State which parasite is depicted.
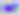
Toxoplasma gondii.

Micrograph. Captured at 400x magnification.